Locate every Plasmodium parasite.
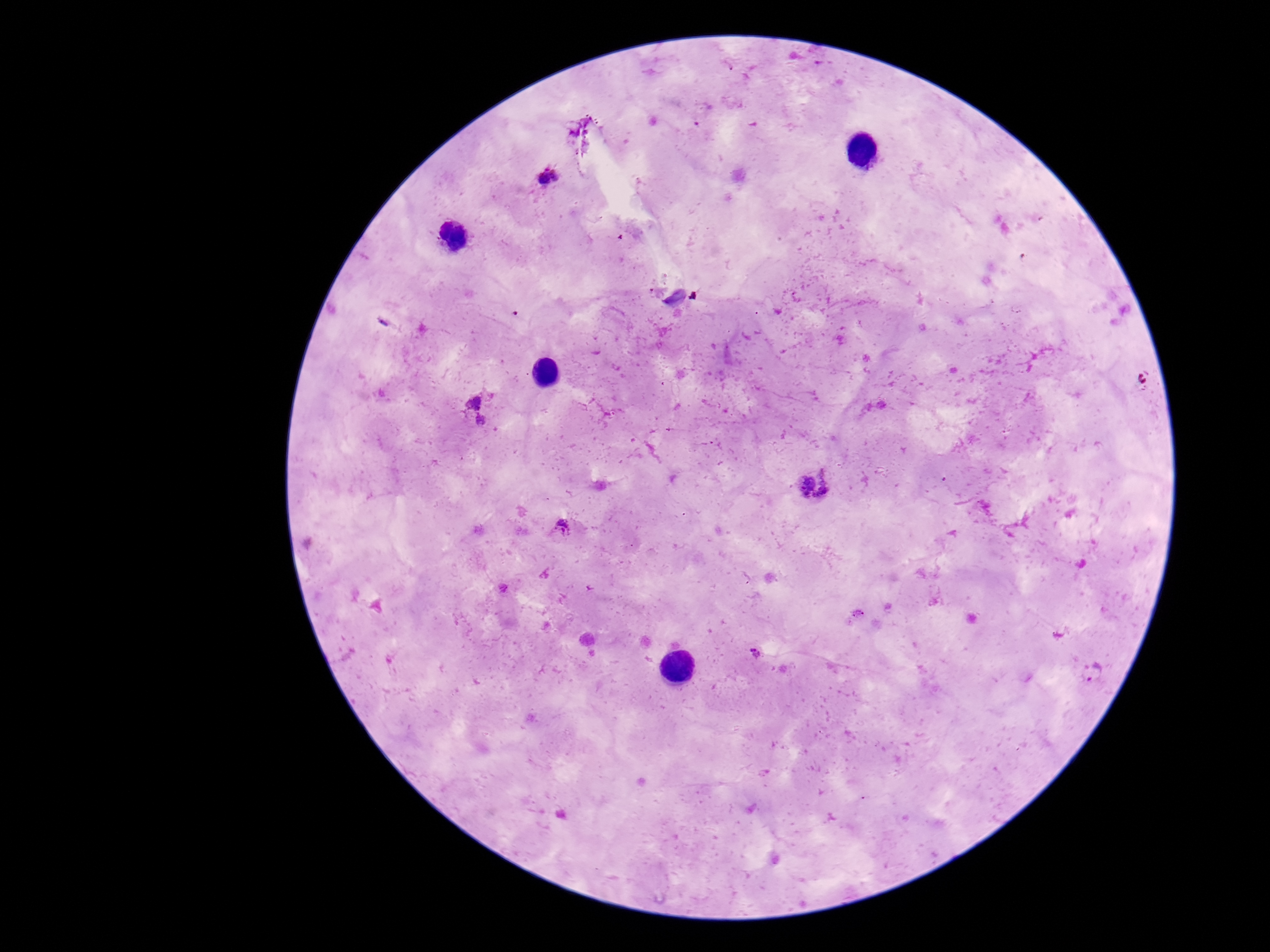
Approximate centers as (x, y) in pixels.
Plasmodium parasites: (549, 177), (477, 412), (813, 485), (563, 526), (858, 614), (756, 652), (1095, 672).

capture = smartphone camera through the microscope eyepiece
field of view = single
magnification = 100x
image size = 1270×952 pixels
preparation = thick blood smear
patient malaria status = positive
stain = Giemsa